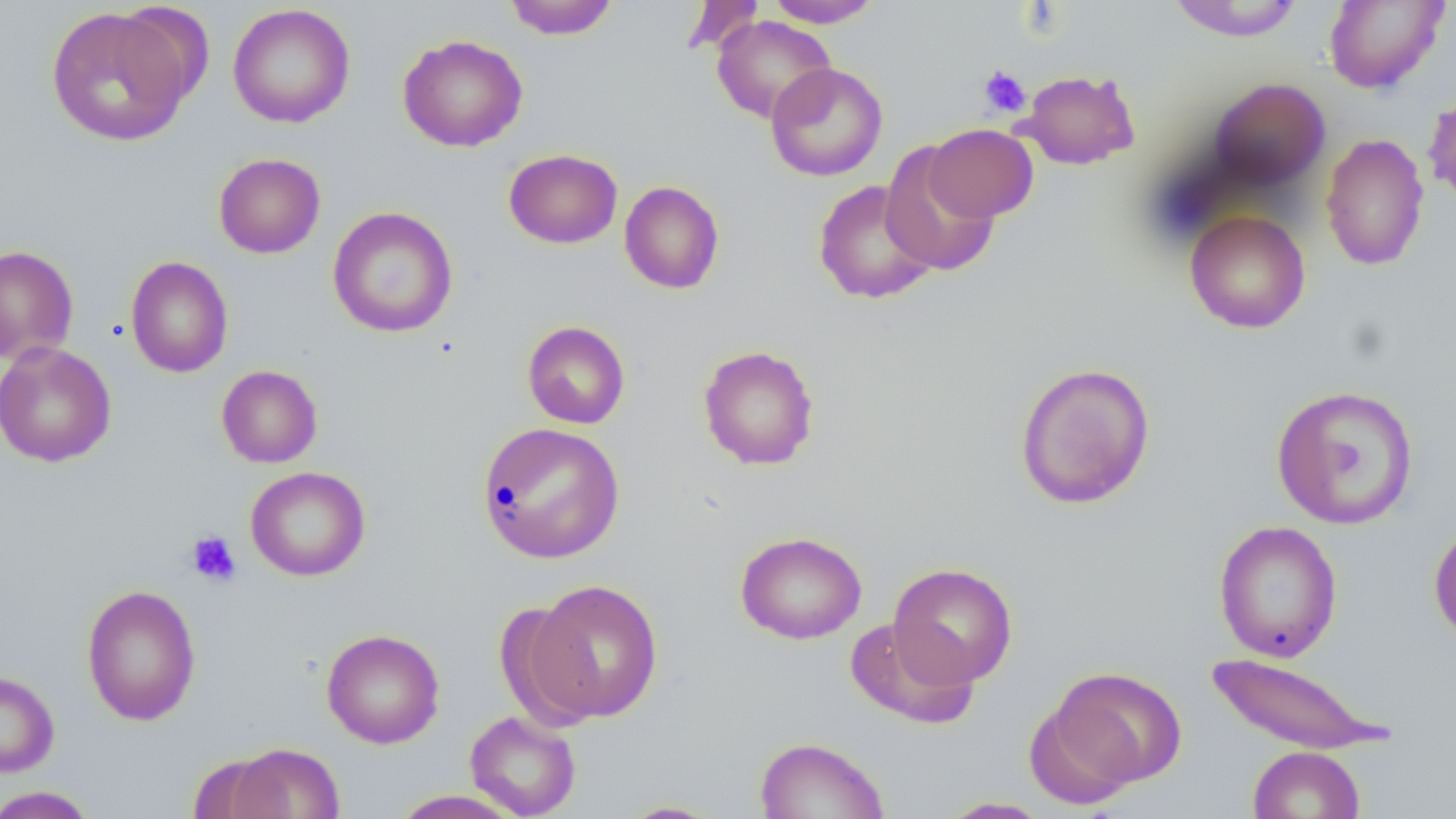

Summary:
  - Coordinate format: approximate bounding boxes as (x1,y1)-(x2,y2) corner pairs in pixels
  - Uninfected red blood cell locations: (503,0)-(620,39), (680,0)-(765,56), (764,0)-(883,27), (1167,0)-(1306,41), (1323,1)-(1449,94), (227,3)-(355,128), (45,6)-(193,147), (712,15)-(836,124), (397,34)-(527,152), (765,62)-(888,181), (1017,68)-(1140,170), (1207,77)-(1330,192), (1422,86)-(1456,208), (923,123)-(1039,222), (1319,133)-(1430,271), (880,143)-(1000,277), (503,148)-(623,249), (213,153)-(326,258), (813,179)-(939,305), (619,180)-(725,294), (327,206)-(458,338), (1184,210)-(1311,333), (0,245)-(79,365), (125,255)-(233,378), (522,320)-(631,429), (0,341)-(117,468), (697,344)-(820,470), (1014,361)-(1156,510), (216,364)-(323,468), (1271,384)-(1420,529), (476,421)-(625,564), (245,466)-(370,581), (1213,519)-(1343,662), (1429,519)-(1456,646), (735,531)-(867,644), (888,562)-(1018,688), (529,578)-(665,722), (81,584)-(201,726), (496,600)-(602,732), (845,618)-(979,729), (321,628)-(445,748), (1203,652)-(1392,753), (1044,666)-(1187,795), (0,670)-(60,778), (465,710)-(582,818), (753,736)-(889,819), (224,743)-(344,819), (1248,746)-(1365,819), (189,752)-(287,818), (0,786)-(99,818), (390,790)-(525,818), (935,797)-(1054,818), (615,800)-(728,818)
  - Platelet locations: (978,65)-(1031,118), (186,529)-(241,586)
  - Slide-level diagnosis: negative for blood parasites
  - Field of view: one of a larger specimen
  - Preparation: thin blood smear
  - Modality: light microscopy
  - Magnification: 1000x
  - Stain: May-Grünwald-Giemsa
  - Image size: 1456×819 pixels